Identify the parasite.
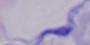
A trypanosome.

modality = micrograph
magnification = 1000x